Assess this cell for malaria.
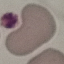
Uninfected.

Acquired by smartphone through the microscope eyepiece. Thin smear of blood. Giemsa-stained preparation. Automatically extracted cell patch, resized to 64 × 64 pixels.